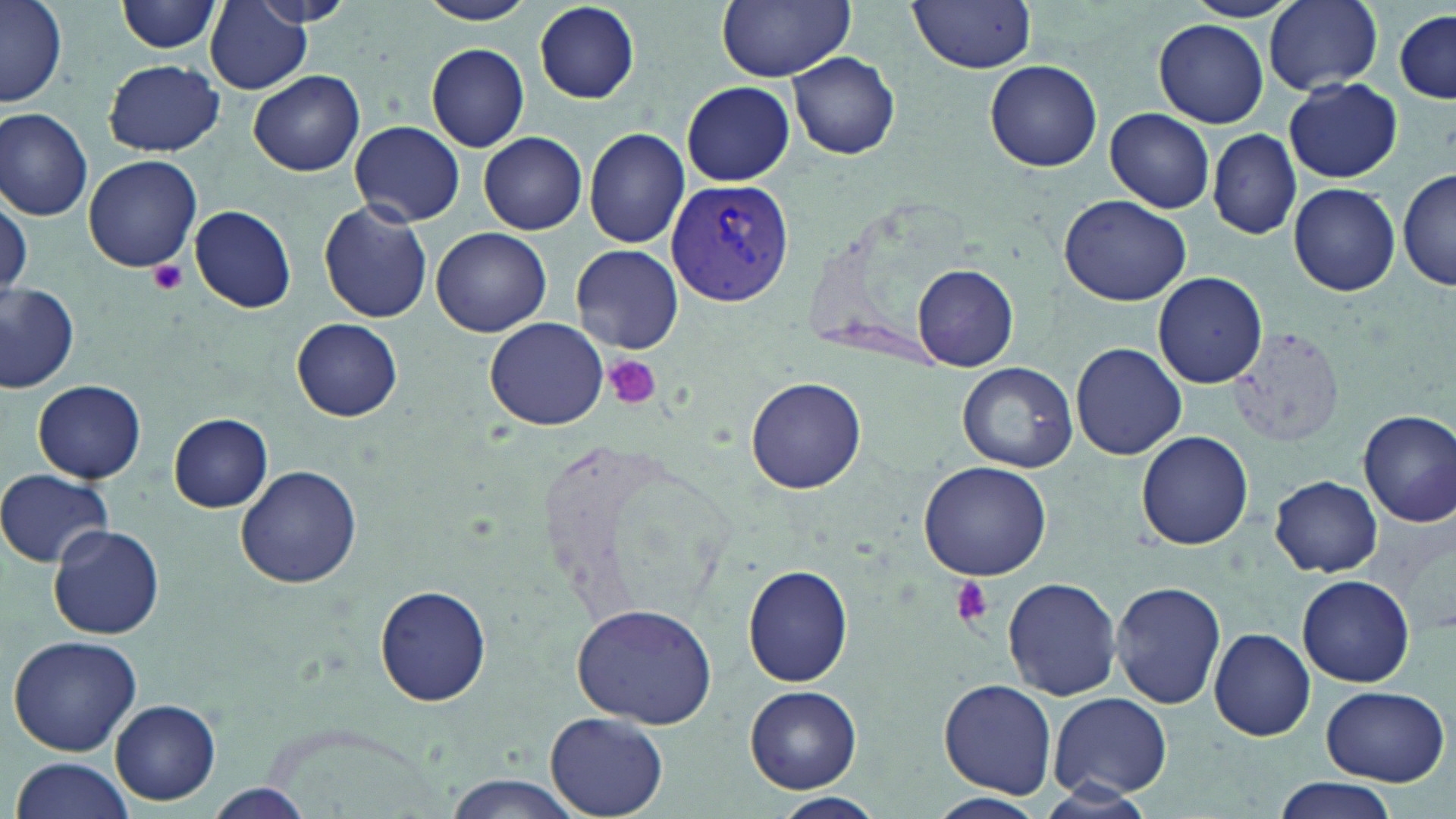
Plasmodium vivax-infected red blood cell locations = approximate bounding boxes as (x1,y1)-(x2,y2) corner pairs in pixels: (665,176)-(795,306)
slide-level diagnosis = Plasmodium vivax
field of view = one of a larger specimen
platelet locations = approximate bounding boxes as (x1,y1)-(x2,y2) corner pairs in pixels: (148,258)-(187,294), (603,354)-(661,411), (948,576)-(990,625)
stain = May-Grünwald-Giemsa
image size = 1456×819 pixels
magnification = 1000x
preparation = thin blood film
modality = optical microscopy
uninfected red blood cell locations = approximate bounding boxes as (x1,y1)-(x2,y2) corner pairs in pixels: (1,0)-(69,107), (116,0)-(222,54), (250,0)-(353,27), (418,0)-(537,25), (715,0)-(856,82), (911,0)-(1037,72), (1264,0)-(1383,93), (532,3)-(641,104), (203,4)-(314,95), (1393,7)-(1454,106), (1153,18)-(1269,128), (425,42)-(530,151), (788,52)-(900,160), (103,59)-(223,156), (985,61)-(1102,171), (247,70)-(366,176), (1282,77)-(1404,183), (683,81)-(795,186), (0,107)-(95,221), (1105,108)-(1214,212), (348,120)-(465,226), (584,127)-(689,247), (1208,128)-(1301,238), (478,132)-(587,234), (83,156)-(201,272), (1399,168)-(1456,292), (1288,182)-(1401,296), (1059,194)-(1191,307), (317,203)-(433,324), (188,206)-(297,314), (432,227)-(552,337), (570,244)-(684,354), (913,264)-(1018,370), (1153,272)-(1267,388), (0,280)-(78,390), (481,317)-(608,430), (292,319)-(403,420), (1070,342)-(1187,461), (956,361)-(1077,474), (747,377)-(866,494), (33,380)-(146,483), (1358,410)-(1456,526), (170,413)-(274,512), (1136,430)-(1254,550), (917,459)-(1055,581), (235,464)-(362,588), (0,470)-(114,568), (1269,476)-(1383,576), (47,525)-(165,640), (743,565)-(854,687), (1298,575)-(1414,688), (1002,577)-(1123,701), (1110,579)-(1229,711), (375,585)-(492,706), (571,603)-(719,728), (1210,627)-(1315,742), (8,635)-(143,756), (940,680)-(1058,798), (745,685)-(862,794), (1320,685)-(1451,786), (1048,691)-(1173,801), (111,699)-(221,805), (545,711)-(668,817), (9,756)-(138,819), (441,775)-(585,819), (1276,780)-(1393,819), (204,786)-(316,818), (775,792)-(884,816), (925,793)-(1048,819)